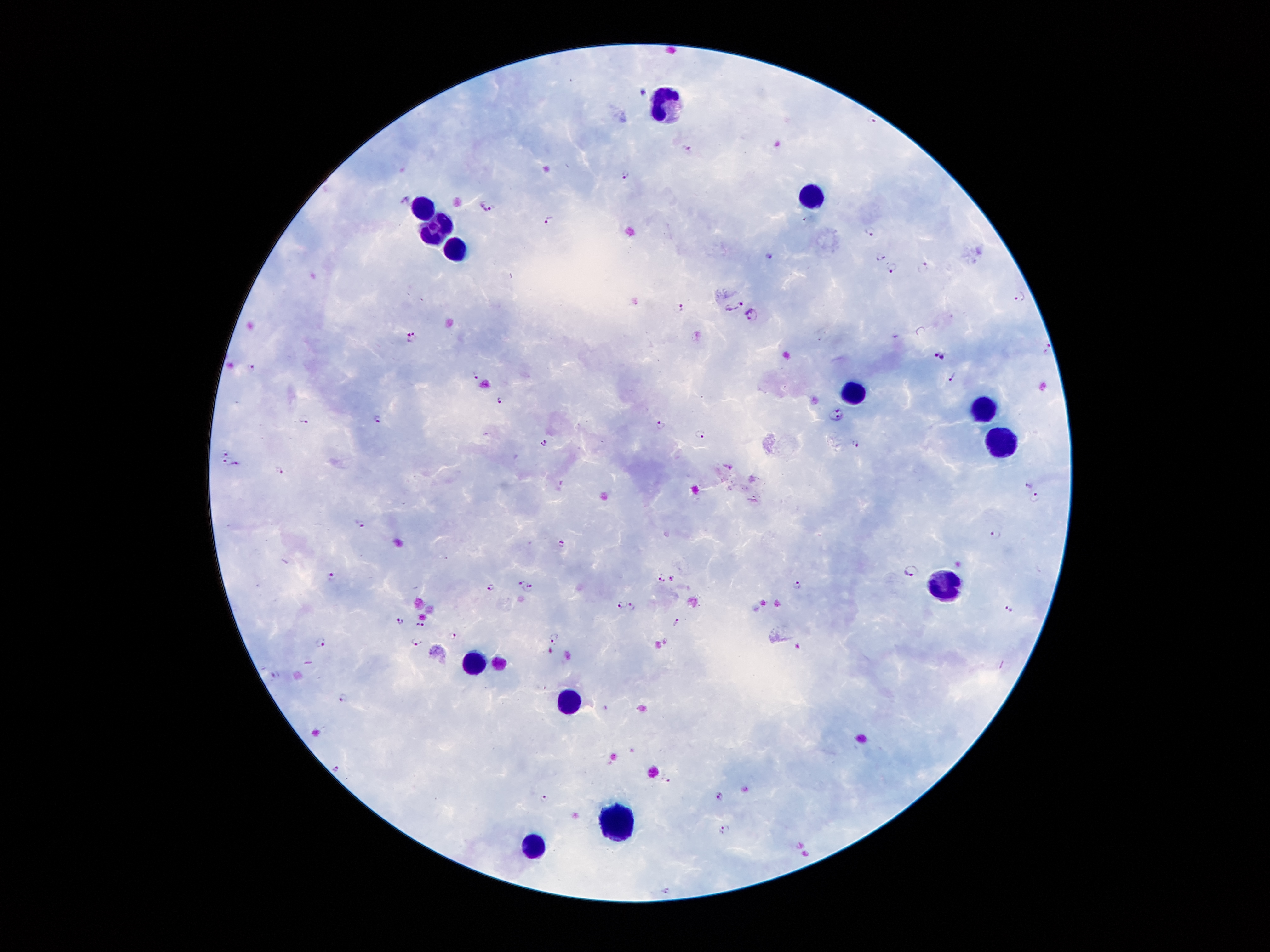
Approximate object centers, in pixels from the top-left corner.
Summary:
  - Leukocyte locations: (x=660, y=100), (x=813, y=196), (x=423, y=203), (x=431, y=228), (x=459, y=248), (x=858, y=394), (x=984, y=408), (x=1005, y=439), (x=945, y=584), (x=474, y=660), (x=569, y=700), (x=614, y=819), (x=535, y=847)
  - Malaria parasite locations: (x=688, y=149), (x=626, y=174), (x=404, y=196), (x=486, y=206), (x=551, y=218), (x=871, y=231), (x=769, y=255), (x=882, y=255), (x=890, y=267), (x=925, y=267), (x=1021, y=296), (x=734, y=304), (x=679, y=308), (x=751, y=314), (x=411, y=336), (x=1048, y=349), (x=934, y=352), (x=944, y=357), (x=252, y=365), (x=477, y=374), (x=955, y=376), (x=499, y=400), (x=837, y=414), (x=304, y=417), (x=376, y=417), (x=662, y=424), (x=699, y=434), (x=544, y=443), (x=856, y=443), (x=227, y=452), (x=225, y=461), (x=239, y=463), (x=280, y=470), (x=1029, y=485), (x=1036, y=497), (x=362, y=523), (x=996, y=534), (x=561, y=543), (x=913, y=570), (x=332, y=575), (x=661, y=577), (x=671, y=579), (x=521, y=582), (x=799, y=585), (x=490, y=587), (x=530, y=590), (x=621, y=604), (x=633, y=607), (x=1010, y=610), (x=400, y=622), (x=675, y=622), (x=418, y=625), (x=453, y=636), (x=553, y=637), (x=415, y=641), (x=320, y=642), (x=797, y=644), (x=550, y=648), (x=273, y=673), (x=343, y=697), (x=339, y=768), (x=666, y=781), (x=719, y=796), (x=544, y=800), (x=724, y=830), (x=667, y=891)
  - Image size: 1270×952 pixels
  - Patient malaria status: infected with Plasmodium falciparum
  - Preparation: thick blood smear
  - Stain: Giemsa
  - Magnification: 100x
  - Capture: smartphone through the microscope eyepiece
  - Field of view: one from this slide